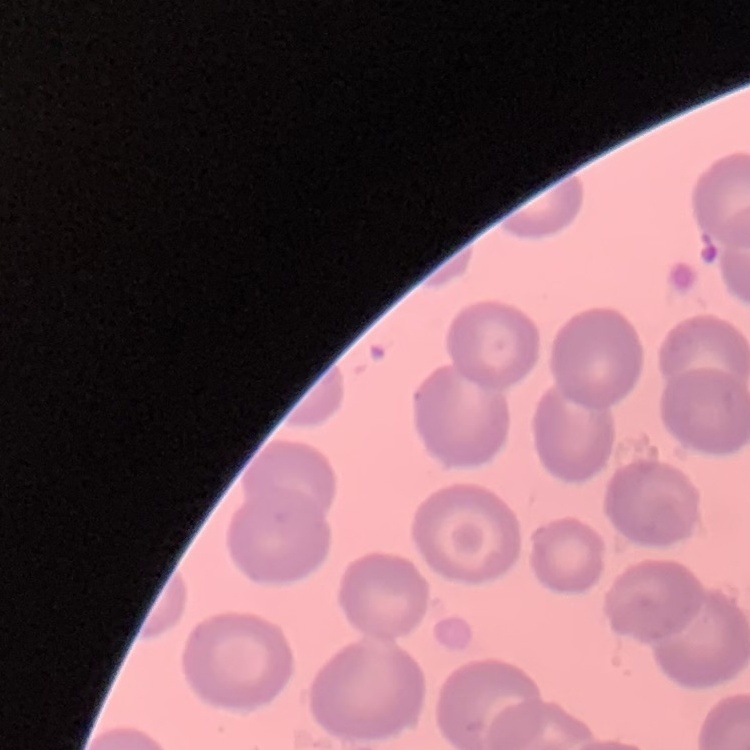 The erythrocytes exhibit no rouleaux formation. Thin blood film. Stained with either Field's or Giemsa. Square crop of a larger photomicrograph.